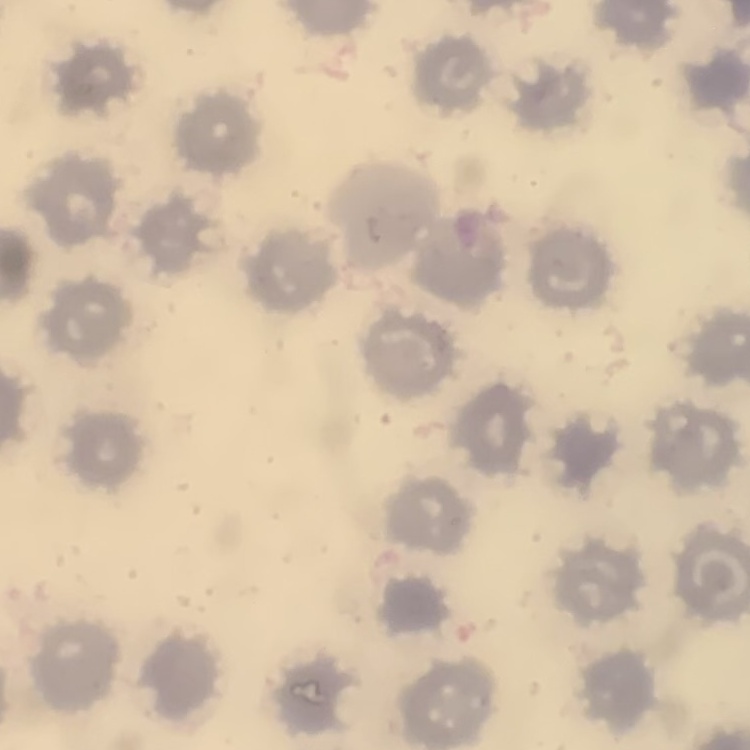
erythrocyte_morphology: no rouleaux formation
stain: Field's or Giemsa
preparation: thin blood film
image_type: square crop of a larger photomicrograph